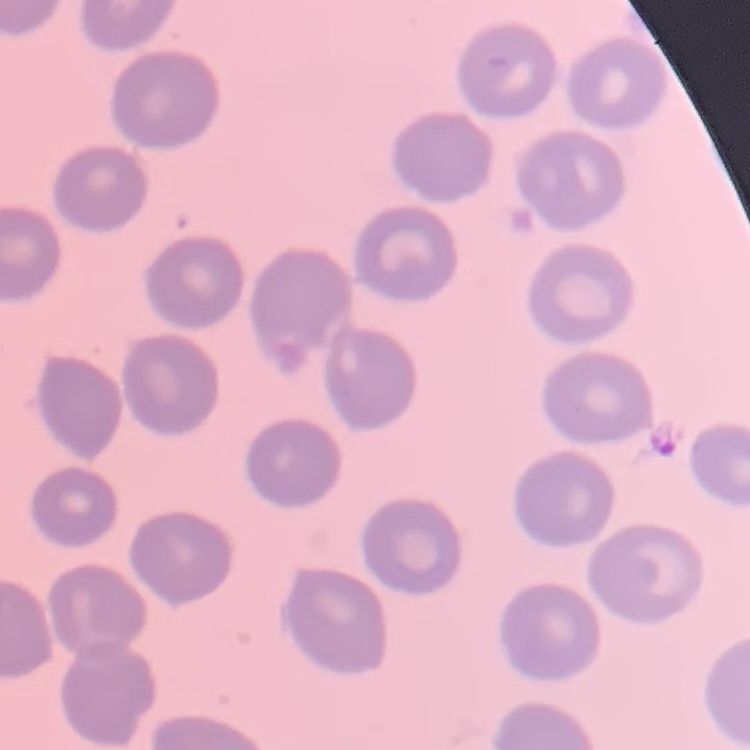 The erythrocytes exhibit no rouleaux formation. One tile cut from a larger photomicrograph. Thin peripheral smear. Field's or Giemsa stain.